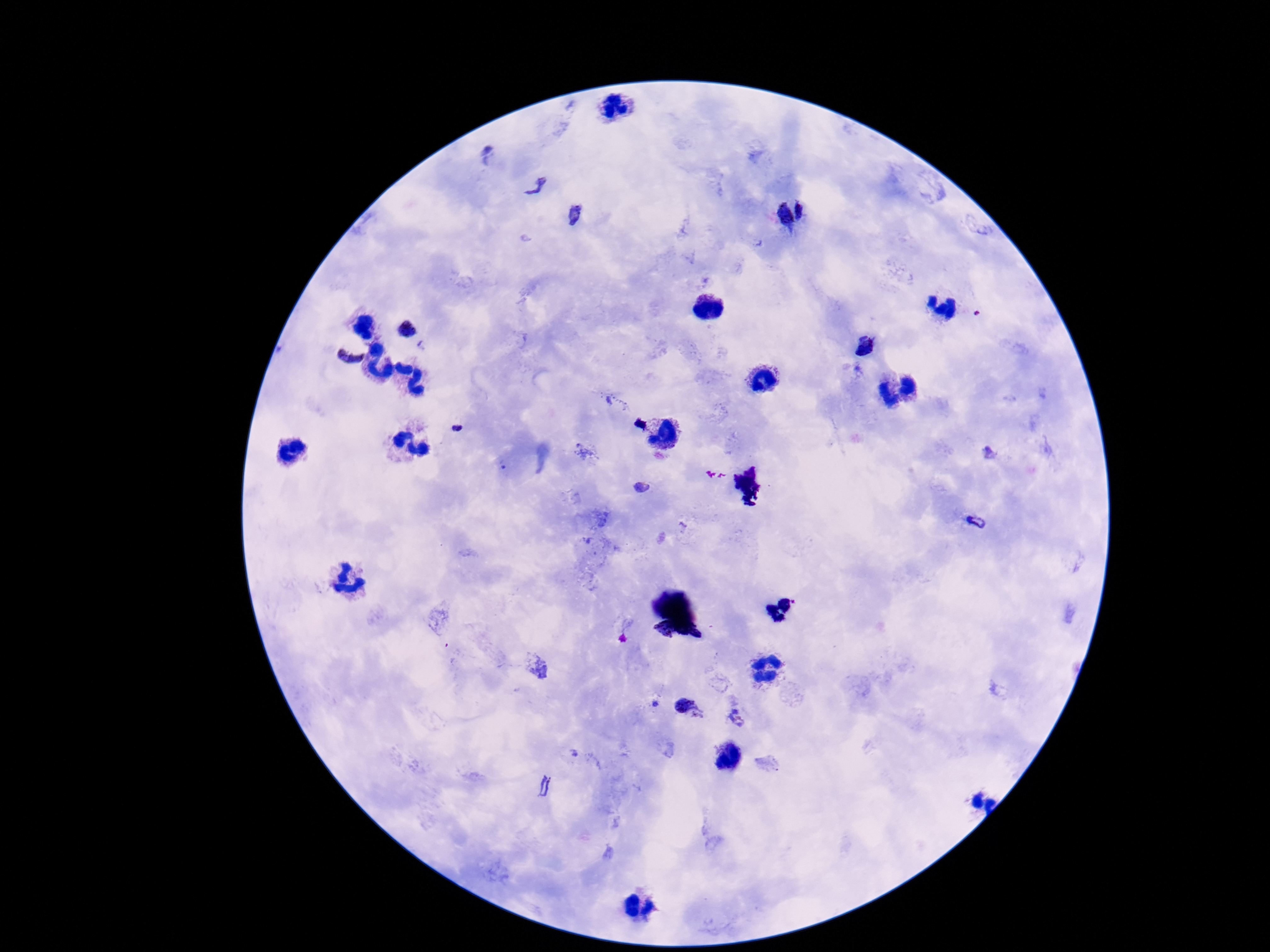

Approximate centers as [x, y] in pixels.
Summary:
  - Plasmodium parasite locations: [538, 186], [576, 214], [349, 356], [991, 455], [640, 487], [975, 521], [687, 709], [736, 717]
  - Preparation: thick blood smear
  - Stain: Giemsa
  - Image size: 1270×952 pixels
  - Capture: smartphone camera through the microscope eyepiece
  - Field of view: one from this slide
  - Patient malaria status: positive
  - Magnification: 100x